Locate every blood parasite and identify its species.
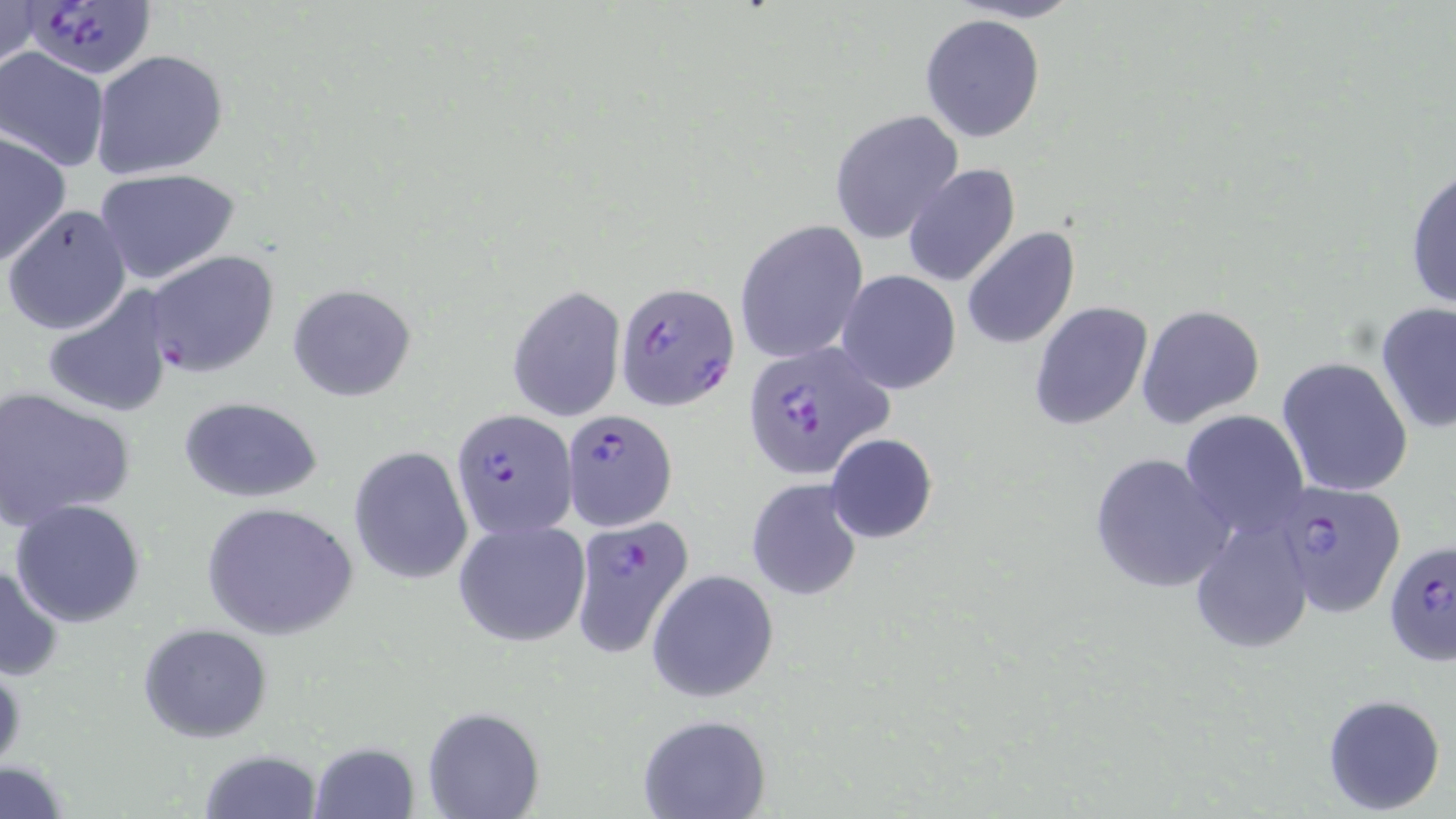
Approximate bounding boxes as named x1/y1/x2/y2 corners in pixels.
Plasmodium falciparum-infected red blood cells: (x1=18, y1=1, x2=155, y2=84), (x1=616, y1=281, x2=740, y2=412), (x1=741, y1=343, x2=894, y2=482), (x1=451, y1=408, x2=578, y2=539), (x1=561, y1=408, x2=678, y2=531), (x1=1270, y1=478, x2=1407, y2=620), (x1=568, y1=516, x2=697, y2=658), (x1=1383, y1=539, x2=1456, y2=666).
No Plasmodium ovale, Plasmodium malariae, Plasmodium vivax, Babesia divergens, or Trypanosoma brucei observed.

Uninfected red blood cell locations: (x1=0, y1=0, x2=41, y2=76), (x1=919, y1=13, x2=1045, y2=144), (x1=0, y1=47, x2=112, y2=172), (x1=90, y1=49, x2=229, y2=179), (x1=831, y1=110, x2=965, y2=244), (x1=0, y1=131, x2=74, y2=268), (x1=1405, y1=161, x2=1455, y2=312), (x1=903, y1=165, x2=1021, y2=287), (x1=93, y1=168, x2=241, y2=285), (x1=2, y1=204, x2=133, y2=337), (x1=735, y1=220, x2=868, y2=365), (x1=963, y1=227, x2=1079, y2=350), (x1=144, y1=250, x2=279, y2=377), (x1=836, y1=271, x2=962, y2=394), (x1=287, y1=283, x2=417, y2=402), (x1=41, y1=285, x2=176, y2=420), (x1=507, y1=287, x2=626, y2=422), (x1=1029, y1=301, x2=1152, y2=432), (x1=1376, y1=302, x2=1456, y2=433), (x1=1137, y1=304, x2=1265, y2=430), (x1=1276, y1=357, x2=1414, y2=498), (x1=0, y1=387, x2=137, y2=528), (x1=177, y1=396, x2=325, y2=503), (x1=1180, y1=410, x2=1309, y2=535), (x1=826, y1=433, x2=938, y2=543), (x1=348, y1=445, x2=473, y2=585), (x1=1089, y1=452, x2=1231, y2=593), (x1=746, y1=478, x2=863, y2=601), (x1=9, y1=499, x2=148, y2=628), (x1=201, y1=502, x2=357, y2=639), (x1=1190, y1=515, x2=1315, y2=654), (x1=452, y1=517, x2=591, y2=647), (x1=0, y1=559, x2=65, y2=681), (x1=647, y1=569, x2=779, y2=703), (x1=138, y1=624, x2=272, y2=743), (x1=0, y1=660, x2=25, y2=773), (x1=1321, y1=693, x2=1447, y2=815), (x1=423, y1=706, x2=544, y2=819), (x1=638, y1=714, x2=769, y2=819), (x1=308, y1=742, x2=421, y2=819), (x1=198, y1=748, x2=322, y2=819), (x1=0, y1=762, x2=74, y2=816). Slide-level diagnosis: Plasmodium falciparum. Image is 1456×819 pixels. Light microscopy. May-Grünwald-Giemsa stain. 1000x magnification. Single field of view. Thin blood film.